Describe the morphology of the erythrocytes.
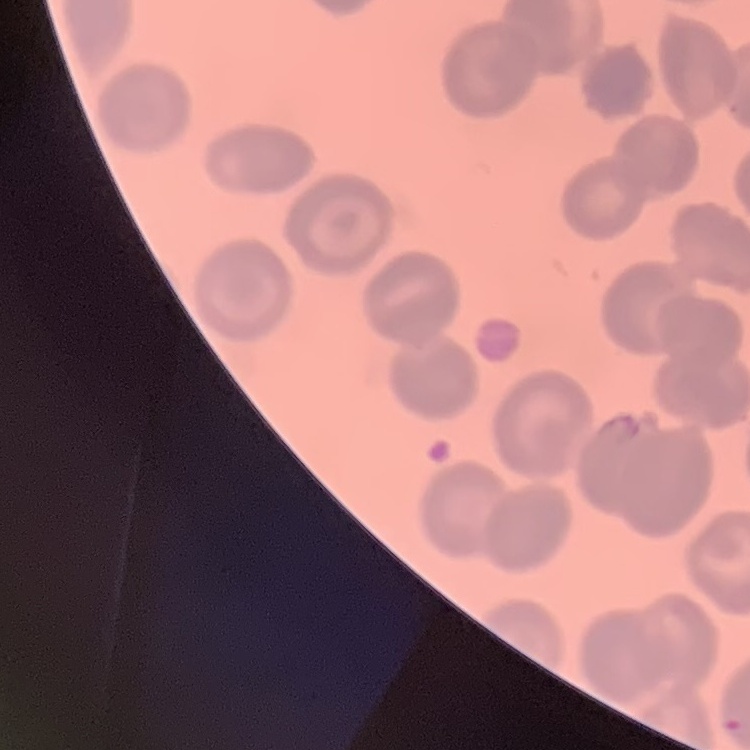

They show no rouleaux formation.

image type = one tile cut from a larger photomicrograph
stain = Field's or Giemsa
preparation = thin blood film